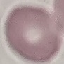
Result: negative for malaria parasites. Giemsa stain. Cell patch, automatically extracted from a larger field of view and resized to 64 × 64 pixels. Acquired by smartphone through the microscope eyepiece. Thin blood film.